Assess this cell for malaria.
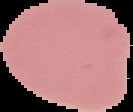
It is uninfected.

image size = 133×112 pixels
image type = segmented cell region on a black background
preparation = thin blood smear